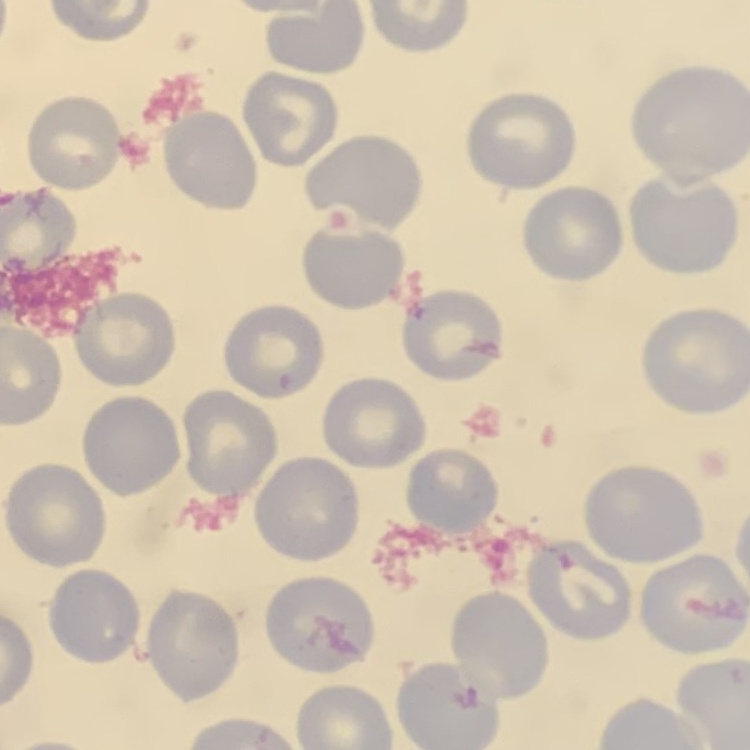

Summary:
  - Erythrocyte morphology: no rouleaux formation
  - Image type: square crop of a larger photomicrograph
  - Stain: Field's or Giemsa
  - Preparation: thin blood smear